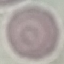

Result: negative for malaria parasites. Automatically extracted cell patch, resized to 64 × 64 pixels. Giemsa stain. Thin blood smear. Acquired by smartphone through the microscope eyepiece.